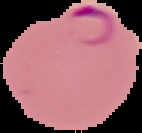
Summary:
  - Image type: segmented cell region on a black background
  - Malaria status: parasitized
  - Image size: 142×133 pixels
  - Preparation: thin blood smear